Report the malaria status.
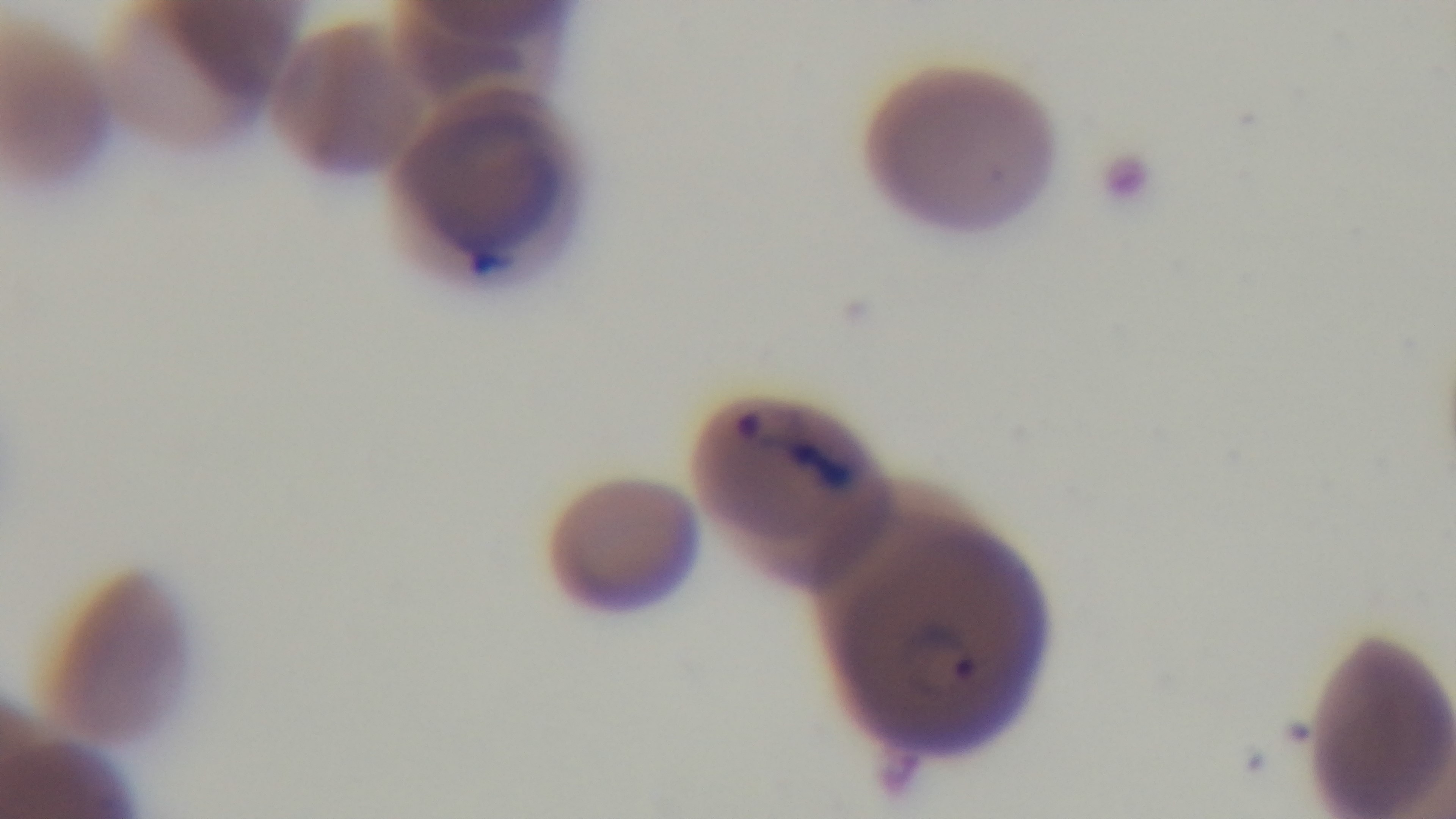

Positive.

Summary:
  - Objective: 100x oil immersion
  - Modality: light microscopy
  - Field of view: one from the slide
  - Capture: mounted 4K digital camera
  - Preparation: thin smear
  - Stain: Giemsa